Report the malaria status of this cell.
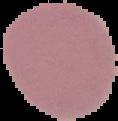

It is uninfected.

Image is 118×121 pixels. From a thin blood film. Cell region segmented out of the field of view; the surrounding area is masked to black.